Outline each Plasmodium falciparum-infected red blood cell.
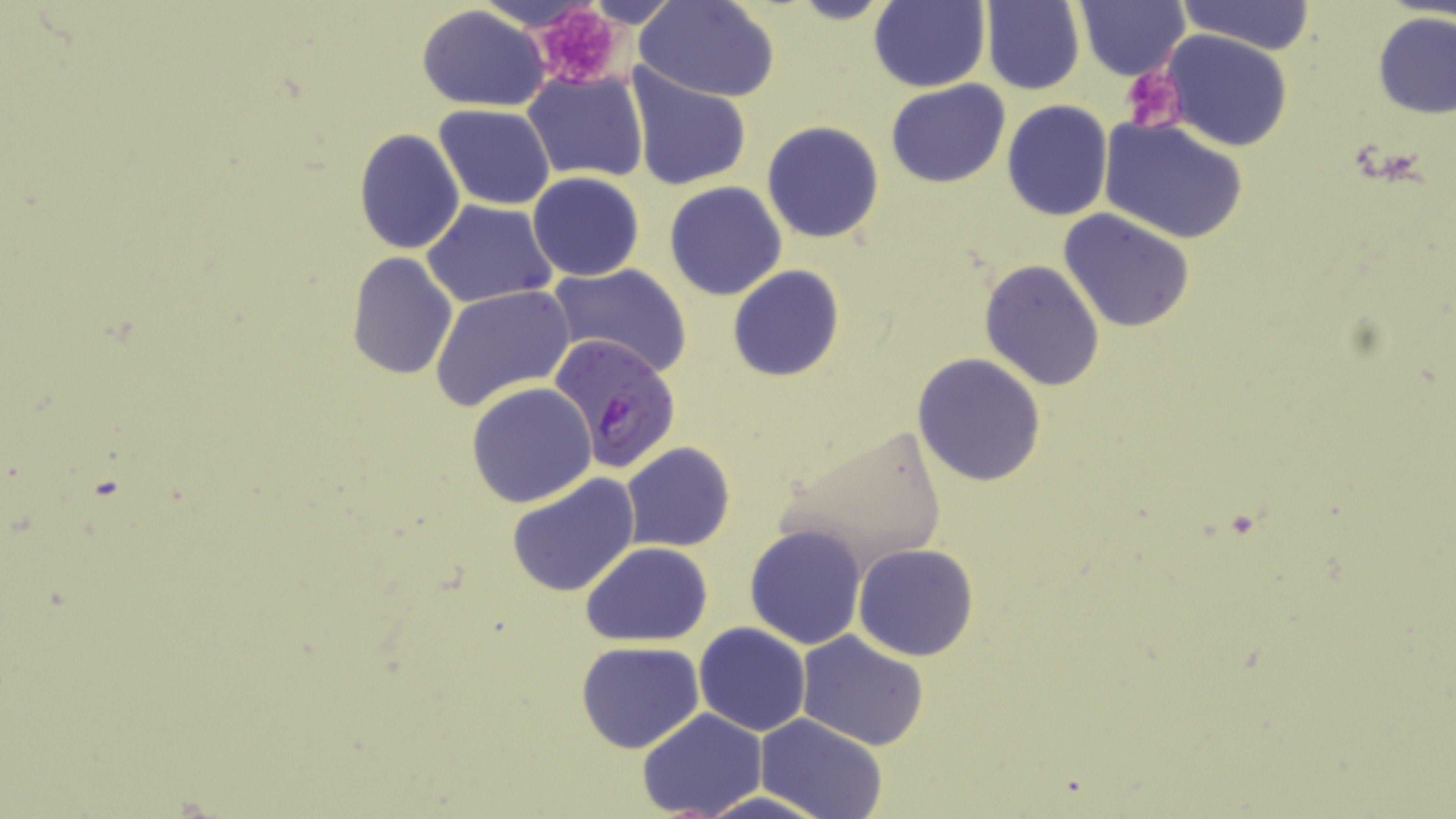

Approximate bounding boxes as named x1/y1/x2/y2 corners in pixels.
Plasmodium falciparum-infected red blood cells: (x1=548, y1=332, x2=680, y2=473).

slide-level diagnosis = Plasmodium falciparum
preparation = thin blood smear
stain = May-Grünwald-Giemsa
modality = optical microscopy
magnification = 1000x
field of view = one of a larger specimen
platelet locations = approximate bounding boxes as named x1/y1/x2/y2 corners in pixels: (x1=529, y1=6, x2=626, y2=90), (x1=1122, y1=66, x2=1187, y2=135)
uninfected red blood cell locations = approximate bounding boxes as named x1/y1/x2/y2 corners in pixels: (x1=788, y1=0, x2=898, y2=25), (x1=1077, y1=0, x2=1191, y2=81), (x1=1176, y1=0, x2=1314, y2=54), (x1=636, y1=1, x2=780, y2=100), (x1=867, y1=1, x2=990, y2=91), (x1=981, y1=1, x2=1084, y2=93), (x1=416, y1=6, x2=552, y2=110), (x1=1373, y1=12, x2=1456, y2=119), (x1=1162, y1=31, x2=1293, y2=151), (x1=623, y1=65, x2=752, y2=192), (x1=523, y1=70, x2=649, y2=183), (x1=885, y1=79, x2=1010, y2=188), (x1=1003, y1=100, x2=1113, y2=220), (x1=433, y1=104, x2=557, y2=209), (x1=1100, y1=118, x2=1248, y2=244), (x1=762, y1=120, x2=885, y2=243), (x1=353, y1=127, x2=465, y2=255), (x1=527, y1=172, x2=645, y2=281), (x1=663, y1=182, x2=787, y2=301), (x1=423, y1=200, x2=559, y2=308), (x1=1060, y1=209, x2=1196, y2=333), (x1=346, y1=252, x2=459, y2=380), (x1=366, y1=257, x2=529, y2=403), (x1=980, y1=259, x2=1106, y2=390), (x1=545, y1=263, x2=694, y2=379), (x1=727, y1=265, x2=846, y2=381), (x1=431, y1=284, x2=574, y2=410), (x1=912, y1=352, x2=1047, y2=486), (x1=466, y1=382, x2=598, y2=508), (x1=776, y1=425, x2=950, y2=571), (x1=622, y1=443, x2=734, y2=551), (x1=506, y1=472, x2=640, y2=595), (x1=745, y1=523, x2=867, y2=649), (x1=581, y1=542, x2=713, y2=645), (x1=853, y1=544, x2=980, y2=662), (x1=694, y1=622, x2=811, y2=736), (x1=796, y1=632, x2=930, y2=750), (x1=576, y1=641, x2=704, y2=752), (x1=636, y1=709, x2=766, y2=818), (x1=757, y1=714, x2=889, y2=819), (x1=690, y1=790, x2=838, y2=819)
image size = 1456×819 pixels